State the blood parasite species.
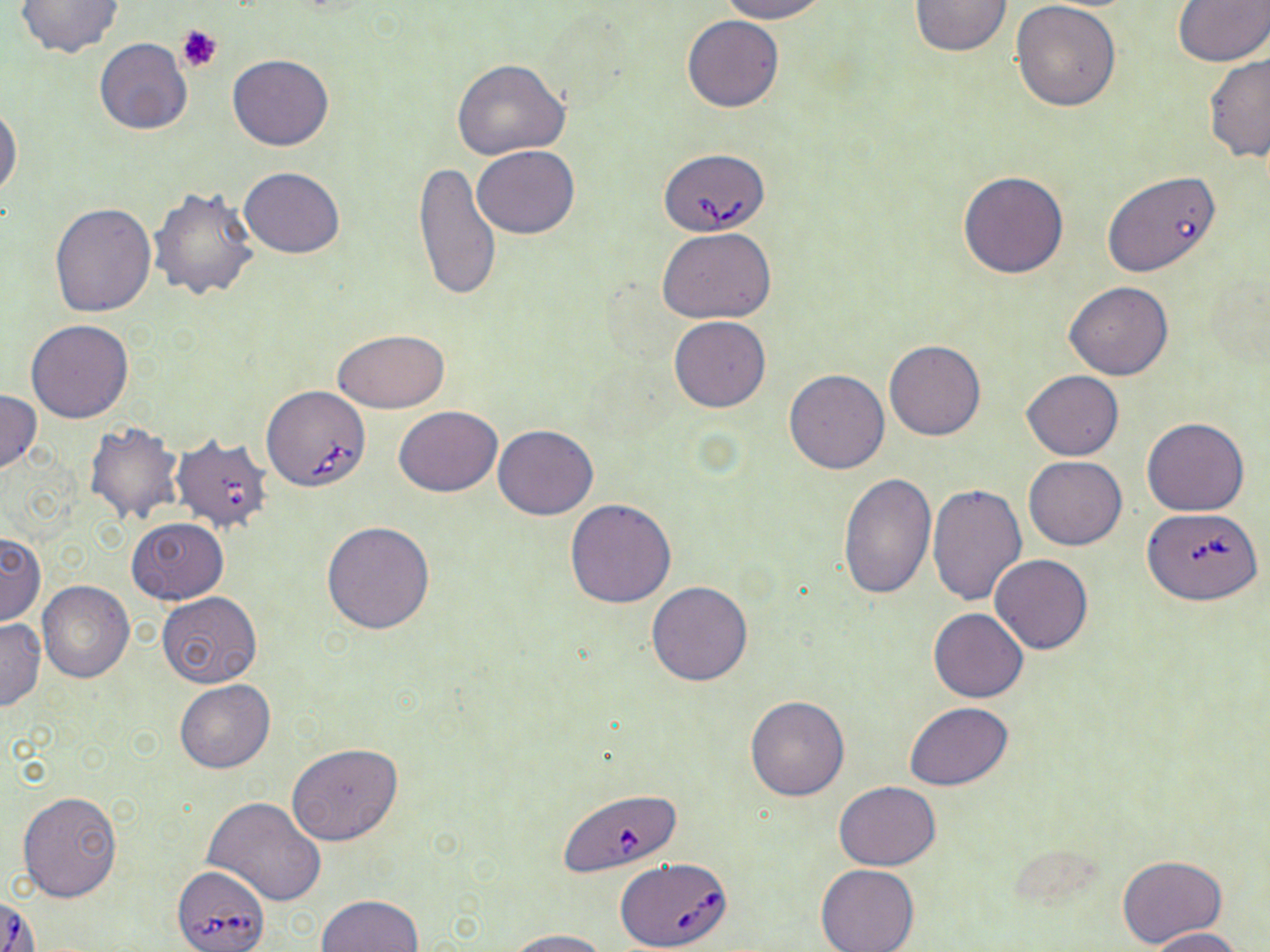

Babesia divergens.

field_of_view: one of a larger specimen
modality: light microscopy
image_size: 1270×952 pixels
magnification: 1000x
stain: May-Grünwald-Giemsa
preparation: thin blood film
babesia_divergens_infected_red_blood_cell_locations: 'approximate bounding boxes as named x1/y1/x2/y2 corners in pixels: (x1=660, y1=148, x2=770, y2=236), (x1=261, y1=385, x2=371, y2=493), (x1=167, y1=435, x2=276, y2=540), (x1=1144, y1=513, x2=1263, y2=609), (x1=562, y1=786, x2=681, y2=878), (x1=616, y1=859, x2=733, y2=950), (x1=172, y1=864, x2=270, y2=952)'
platelet_locations: 'approximate bounding boxes as named x1/y1/x2/y2 corners in pixels: (x1=176, y1=24, x2=222, y2=72)'
uninfected_red_blood_cell_locations: 'approximate bounding boxes as named x1/y1/x2/y2 corners in pixels: (x1=15, y1=0, x2=123, y2=57), (x1=716, y1=0, x2=828, y2=23), (x1=908, y1=0, x2=1014, y2=57), (x1=1012, y1=0, x2=1122, y2=111), (x1=1173, y1=0, x2=1270, y2=66), (x1=682, y1=14, x2=783, y2=112), (x1=95, y1=38, x2=193, y2=135), (x1=1203, y1=52, x2=1270, y2=161), (x1=227, y1=53, x2=334, y2=151), (x1=452, y1=58, x2=570, y2=159), (x1=0, y1=103, x2=22, y2=201), (x1=472, y1=145, x2=580, y2=238), (x1=413, y1=162, x2=501, y2=301), (x1=240, y1=166, x2=345, y2=258), (x1=958, y1=170, x2=1070, y2=279), (x1=1103, y1=170, x2=1221, y2=279), (x1=148, y1=185, x2=258, y2=304), (x1=50, y1=202, x2=157, y2=318), (x1=658, y1=227, x2=776, y2=324), (x1=1063, y1=281, x2=1174, y2=380), (x1=669, y1=316, x2=771, y2=412), (x1=26, y1=320, x2=135, y2=423), (x1=333, y1=330, x2=448, y2=414), (x1=885, y1=340, x2=985, y2=440), (x1=785, y1=369, x2=889, y2=473), (x1=1023, y1=370, x2=1123, y2=461), (x1=0, y1=390, x2=42, y2=474), (x1=393, y1=406, x2=502, y2=496), (x1=1142, y1=417, x2=1250, y2=516), (x1=84, y1=421, x2=185, y2=526), (x1=492, y1=424, x2=599, y2=519), (x1=1023, y1=456, x2=1127, y2=550), (x1=837, y1=470, x2=935, y2=599), (x1=927, y1=482, x2=1028, y2=607), (x1=565, y1=498, x2=677, y2=608), (x1=126, y1=517, x2=228, y2=604), (x1=321, y1=520, x2=435, y2=634), (x1=0, y1=532, x2=44, y2=625), (x1=990, y1=554, x2=1093, y2=655), (x1=645, y1=580, x2=752, y2=687), (x1=38, y1=581, x2=134, y2=682), (x1=156, y1=593, x2=264, y2=688), (x1=929, y1=609, x2=1028, y2=702), (x1=0, y1=617, x2=45, y2=710), (x1=175, y1=679, x2=274, y2=773), (x1=745, y1=696, x2=848, y2=801), (x1=905, y1=702, x2=1014, y2=790), (x1=287, y1=744, x2=402, y2=846), (x1=834, y1=781, x2=941, y2=870), (x1=17, y1=790, x2=121, y2=902), (x1=203, y1=797, x2=327, y2=907), (x1=1116, y1=854, x2=1227, y2=949), (x1=816, y1=864, x2=920, y2=952), (x1=317, y1=894, x2=424, y2=952), (x1=1148, y1=927, x2=1245, y2=951), (x1=505, y1=928, x2=612, y2=952)'